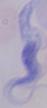

A trypanosome is shown. Micrograph. 1000x magnification.